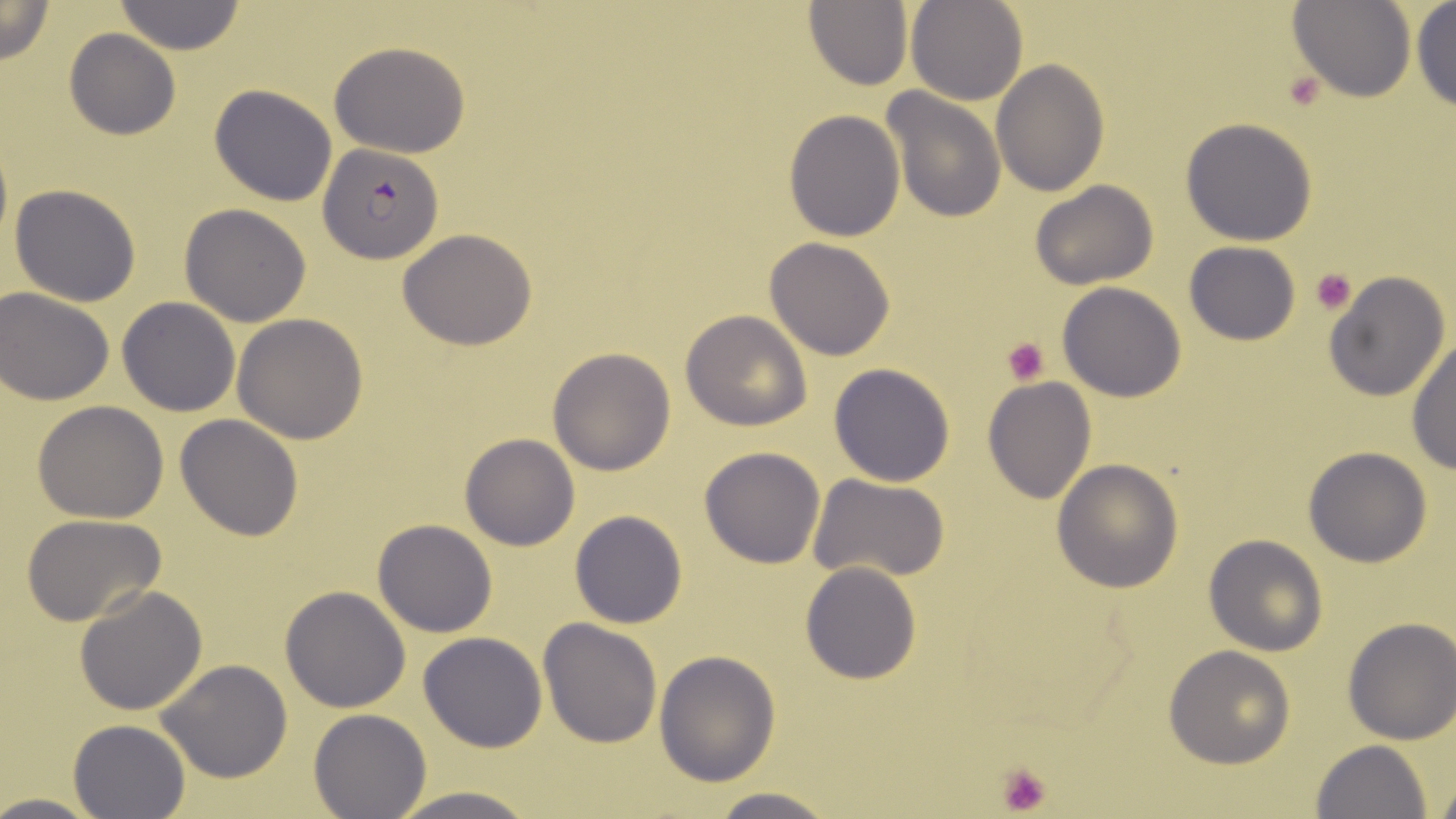

slide-level diagnosis = Plasmodium falciparum
field of view = single
preparation = thin blood film
magnification = 1000x
platelet locations = approximate bounding boxes as (x1, y1, x2, y2) in pixels: (1284, 72, 1324, 111), (1311, 268, 1358, 315), (1002, 338, 1050, 385), (995, 762, 1054, 816)
image size = 1456×819 pixels
Plasmodium falciparum-infected red blood cell locations = approximate bounding boxes as (x1, y1, x2, y2) in pixels: (318, 142, 442, 264)
uninfected red blood cell locations = approximate bounding boxes as (x1, y1, x2, y2) in pixels: (0, 0, 56, 64), (906, 0, 1029, 105), (1290, 0, 1415, 102), (112, 1, 249, 54), (803, 1, 913, 89), (1411, 2, 1456, 114), (64, 28, 181, 141), (328, 40, 471, 159), (990, 59, 1108, 196), (210, 84, 339, 205), (880, 89, 1007, 224), (784, 109, 905, 243), (1180, 118, 1318, 246), (1030, 179, 1158, 289), (8, 183, 142, 307), (178, 203, 312, 326), (398, 229, 538, 349), (765, 236, 896, 360), (1185, 241, 1301, 345), (1323, 272, 1451, 402), (1057, 281, 1188, 403), (1, 285, 117, 404), (117, 296, 241, 417), (680, 311, 812, 431), (232, 313, 369, 444), (1405, 340, 1456, 473), (548, 346, 676, 475), (829, 362, 957, 486), (983, 376, 1097, 504), (33, 400, 169, 522), (176, 413, 306, 541), (459, 432, 580, 550), (699, 446, 827, 568), (1304, 447, 1433, 567), (1051, 458, 1185, 593), (810, 474, 951, 584), (569, 510, 688, 628), (21, 513, 168, 626), (372, 518, 498, 637), (1205, 534, 1329, 657), (800, 561, 922, 683), (75, 584, 208, 716), (281, 585, 412, 714), (1342, 616, 1456, 745), (539, 619, 663, 749), (419, 631, 547, 752), (1163, 645, 1296, 770), (654, 649, 781, 786), (156, 659, 293, 783), (309, 707, 431, 817), (68, 718, 193, 818), (1310, 740, 1433, 819), (1430, 777, 1456, 818), (387, 784, 543, 819), (702, 789, 843, 819), (0, 793, 110, 817)
modality = light microscopy
stain = May-Grünwald-Giemsa